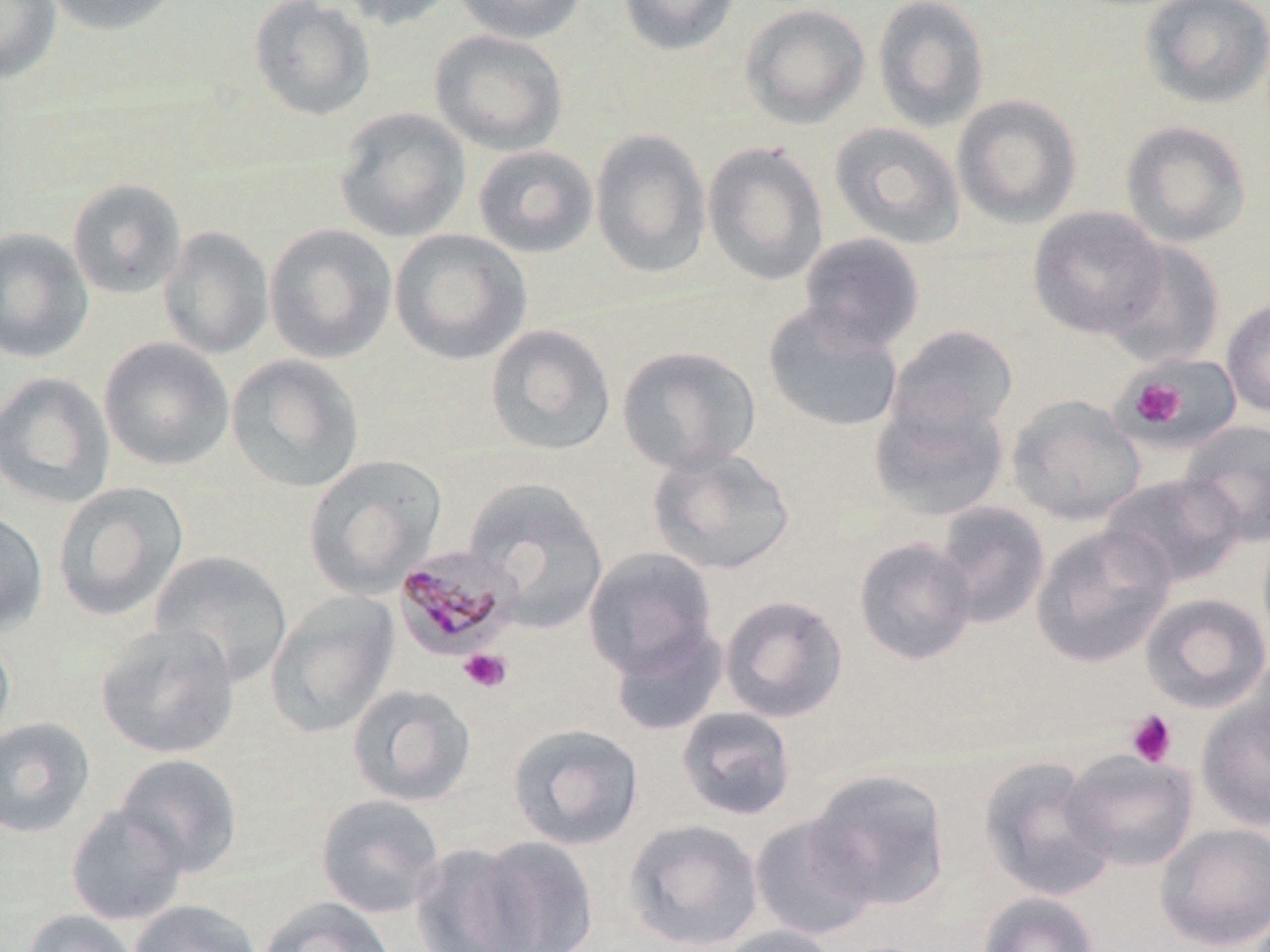

Approximate bounding boxes as (x1,y1)-(x2,y2) corner pairs in pixels. Uninfected red blood cell locations: (41,0)-(183,36), (249,0)-(377,122), (331,0)-(460,31), (451,0)-(589,44), (617,0)-(740,57), (872,0)-(990,132), (1139,0)-(1270,109), (0,1)-(62,85), (740,3)-(870,129), (429,29)-(568,156), (951,93)-(1083,229), (333,107)-(472,243), (1120,120)-(1251,248), (829,122)-(965,249), (589,129)-(712,279), (702,140)-(829,287), (472,144)-(599,259), (67,177)-(188,301), (1028,205)-(1167,340), (264,223)-(398,364), (158,225)-(275,359), (0,228)-(94,364), (389,229)-(532,365), (797,232)-(925,353), (1104,240)-(1226,368), (1221,299)-(1270,418), (762,304)-(905,433), (485,324)-(617,456), (884,324)-(1019,441), (98,337)-(235,472), (617,345)-(761,474), (225,354)-(365,494), (1123,361)-(1233,447), (0,371)-(116,509), (869,394)-(1010,522), (1007,395)-(1146,526), (1179,420)-(1270,546), (648,445)-(796,576), (302,454)-(446,598), (1099,473)-(1245,588), (463,477)-(609,633), (52,482)-(189,622), (932,501)-(1050,630), (0,509)-(49,636), (1030,524)-(1176,668), (853,536)-(977,667), (582,547)-(719,679), (150,550)-(293,688), (264,590)-(399,739), (1139,592)-(1270,714), (719,593)-(849,723), (608,620)-(729,737), (94,622)-(240,760), (0,630)-(15,746), (1244,649)-(1270,774), (346,684)-(476,807), (1195,694)-(1270,832), (676,706)-(797,821), (0,717)-(96,838), (507,723)-(644,851), (1061,748)-(1199,872), (114,753)-(242,877), (979,755)-(1116,901), (806,769)-(950,911), (315,793)-(445,919), (65,803)-(188,926), (749,813)-(880,941), (623,818)-(764,951), (1155,822)-(1270,950), (463,835)-(601,952), (409,841)-(544,951), (976,891)-(1101,952), (257,896)-(396,952), (128,899)-(262,952), (22,908)-(140,952), (714,924)-(843,952). Plasmodium malariae-infected red blood cell locations: (391,546)-(523,662). Platelet locations: (1129,376)-(1187,429), (459,648)-(512,693), (1126,710)-(1177,767). Slide-level diagnosis: Plasmodium malariae. Image is 1270×952 pixels. May-Grünwald-Giemsa-stained preparation. Single field of view. Light microscopy. Thin blood smear. 1000x magnification.